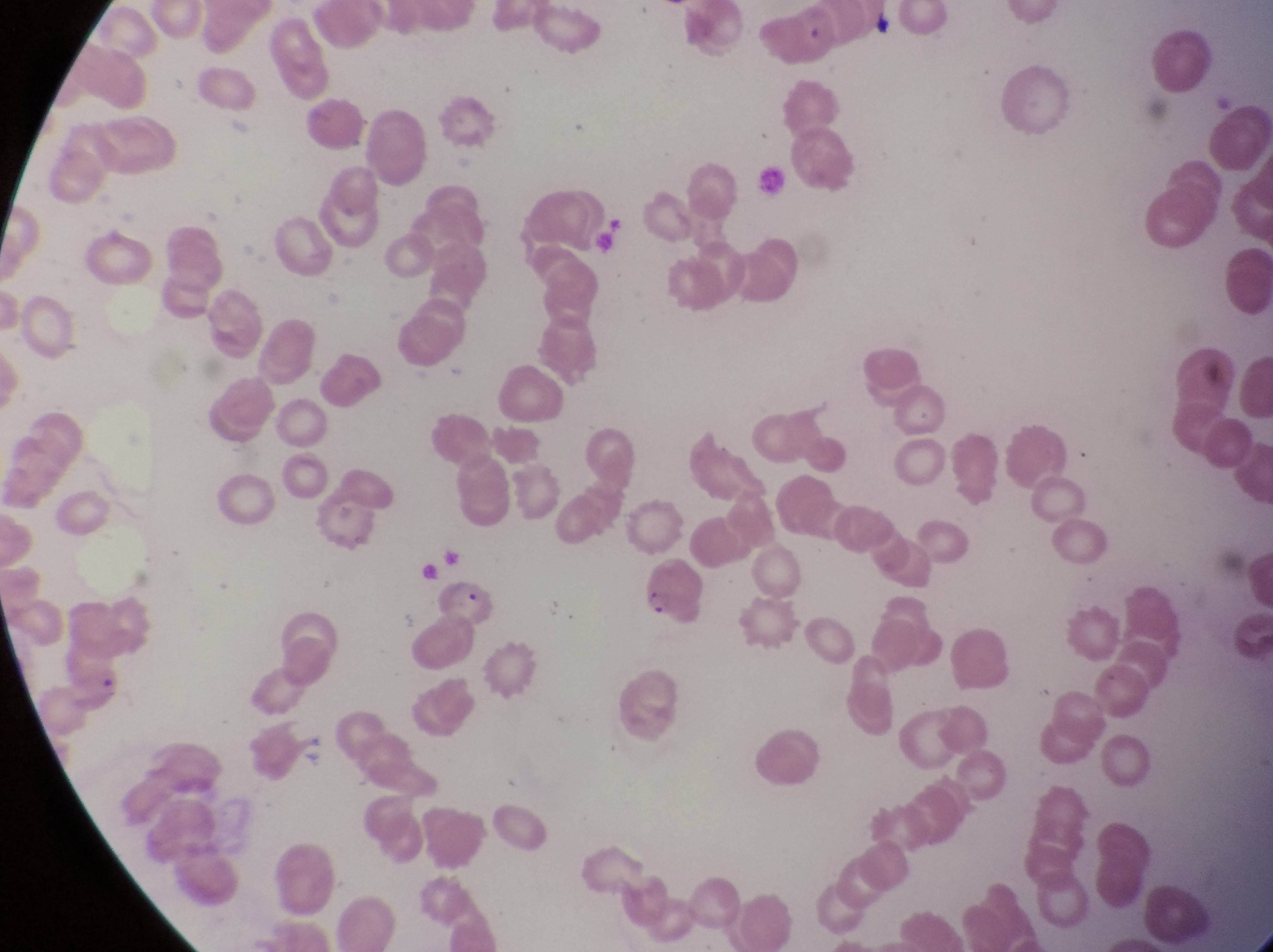
capture = smartphone photograph through the eyepiece of an Olympus CX-23 microscope
parasitised red blood cell locations = approximate bounding boxes as (left, top, right, bottom) in pixels: (641, 561, 706, 621)
field of view = single
image size = 1273×952 pixels
magnification = 1000x
country = Uganda
preparation = thin blood smear